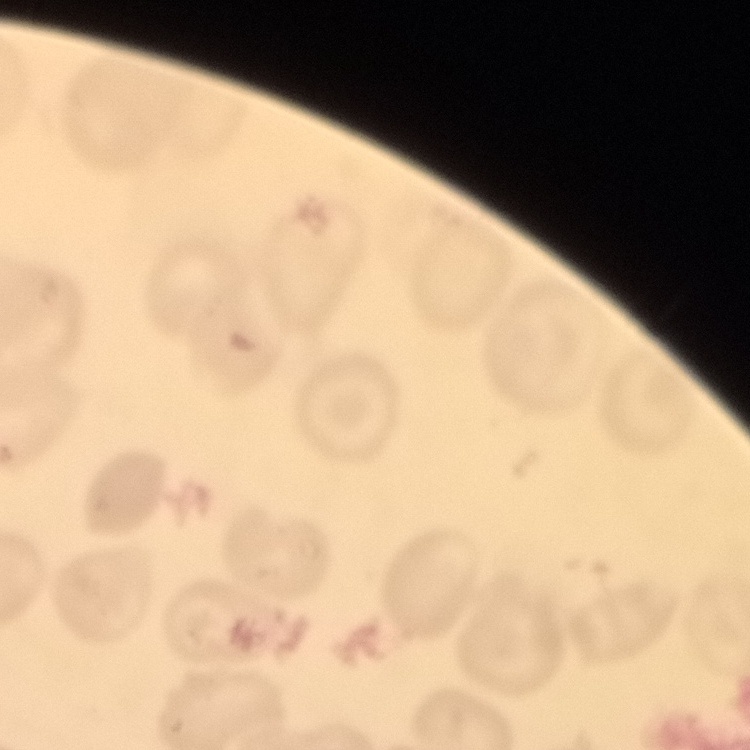

Summary:
  - Red blood cell morphology: no rouleaux formation
  - Image type: square crop of a larger photomicrograph
  - Preparation: thin peripheral smear
  - Stain: Field's or Giemsa